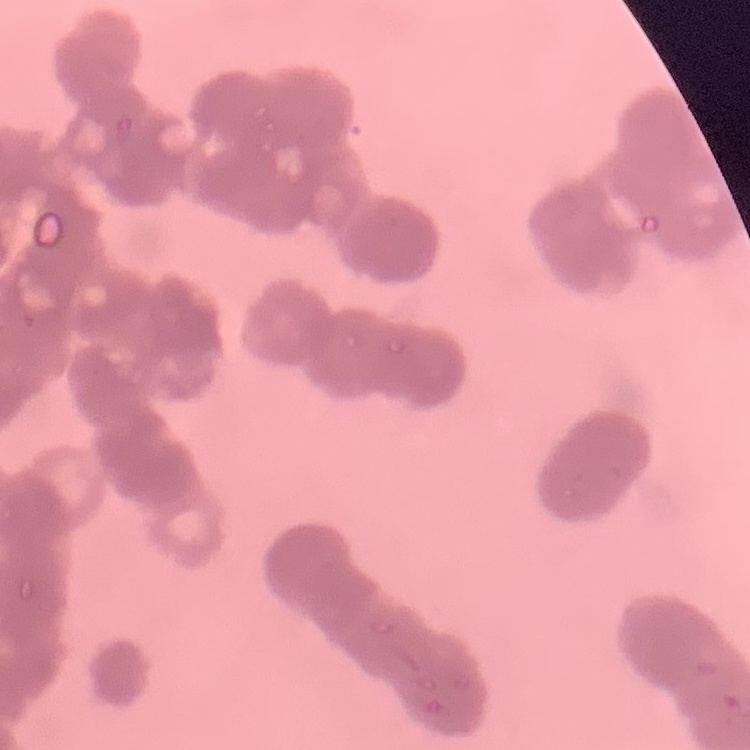

red blood cell morphology = rouleaux formation
preparation = thin peripheral smear
stain = Field's or Giemsa
image type = one tile cut from a larger photomicrograph